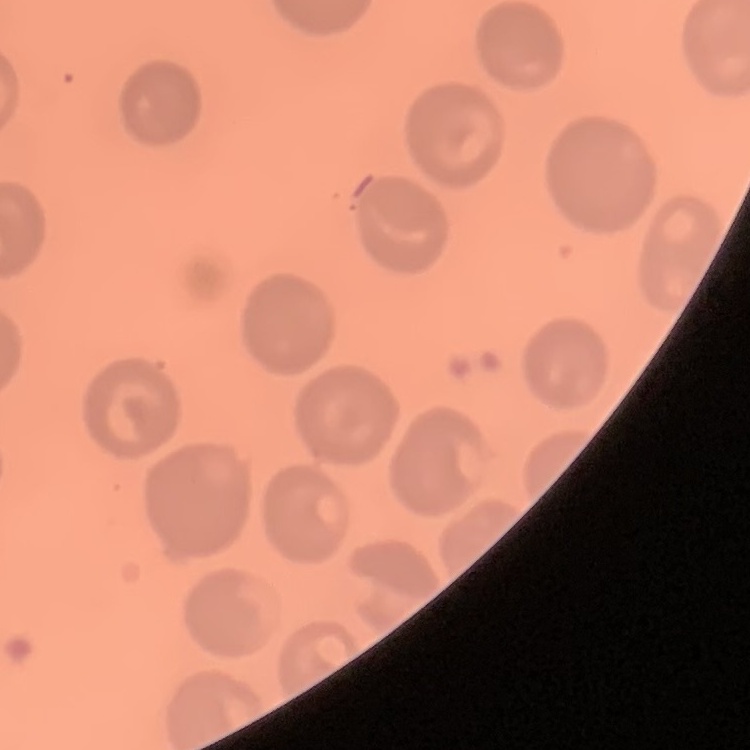
Summary:
  - Red blood cell morphology: no rouleaux formation
  - Preparation: thin blood film
  - Stain: Field's or Giemsa
  - Image type: one tile cut from a larger photomicrograph